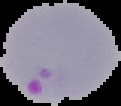

Image is 121×106 pixels. From a thin blood film. Cell region segmented out of the field of view; the surrounding area is masked to black. Malaria status: parasitized.